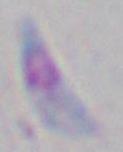

{
  "magnification": "1000x",
  "identification": "Toxoplasma gondii",
  "modality": "micrograph"
}